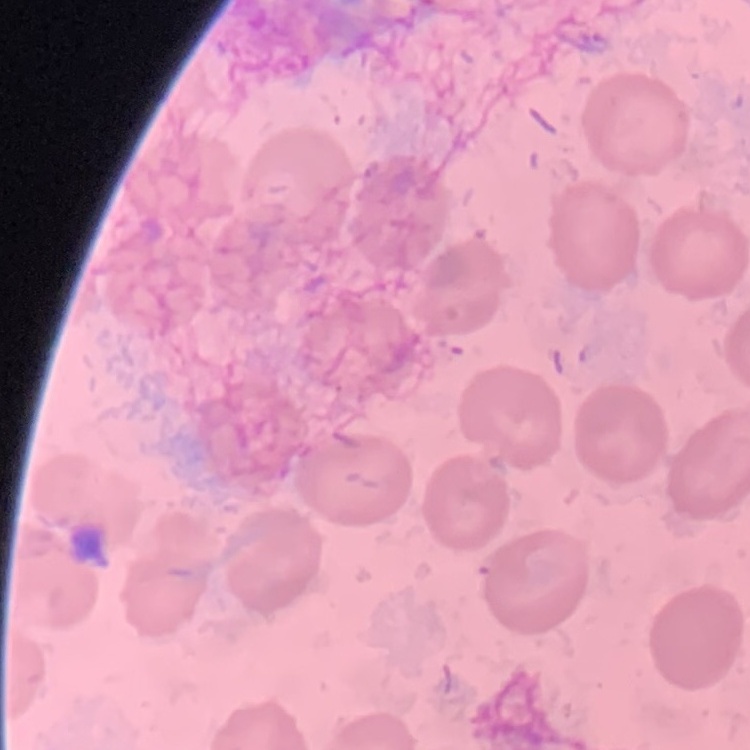
The erythrocytes exhibit no rouleaux formation. One tile cut from a larger photomicrograph. Stained with either Field's or Giemsa. Thin blood film.